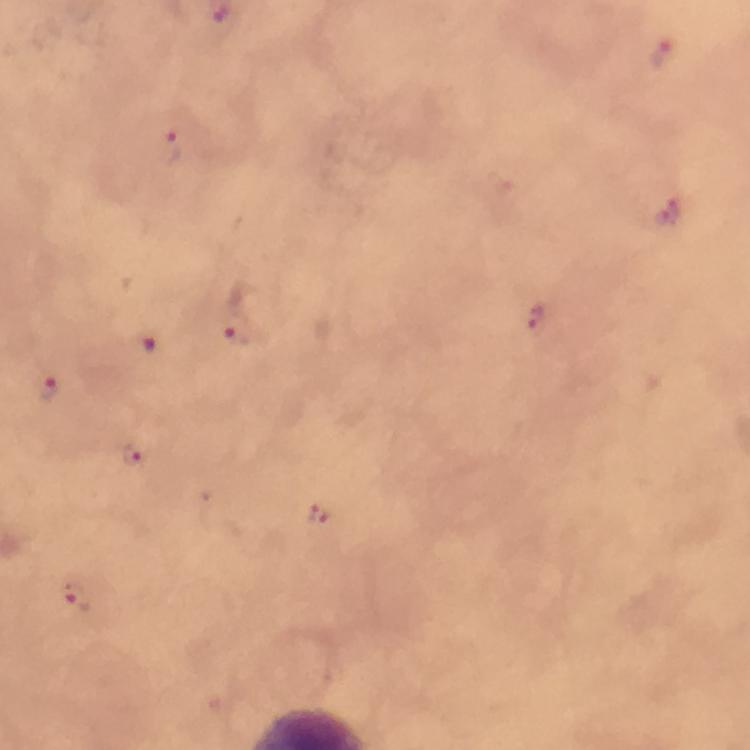
Approximate centers as [x, y] in pixels.
Summary:
  - Malaria parasite locations: [662, 53], [172, 145], [669, 212], [541, 323], [233, 335], [144, 346], [50, 388], [133, 454], [317, 514], [77, 598]
  - Stain: Giemsa
  - Preparation: thick blood film
  - Magnification: 100x
  - Immersion oil: used
  - Capture: smartphone camera through the microscope
  - Context: from a diagnostic examination for malaria
  - Image size: 750×750 pixels
  - Cropped from: one field of view